Describe the morphology of the red blood cells.
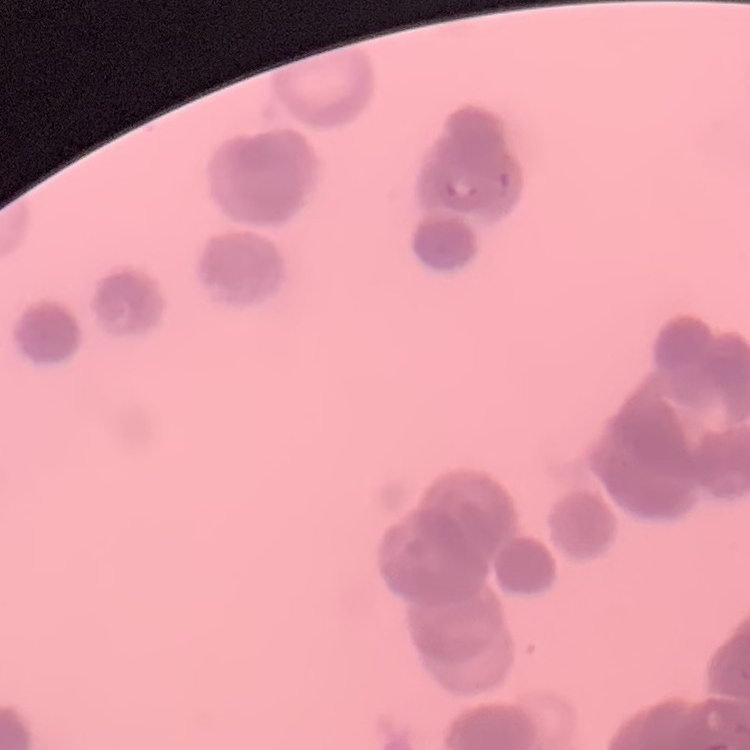
Rouleaux formation.

preparation = thin blood smear
image type = one tile cut from a larger photomicrograph
stain = Field's or Giemsa